Give a bounding box for every parasitised red blood cell.
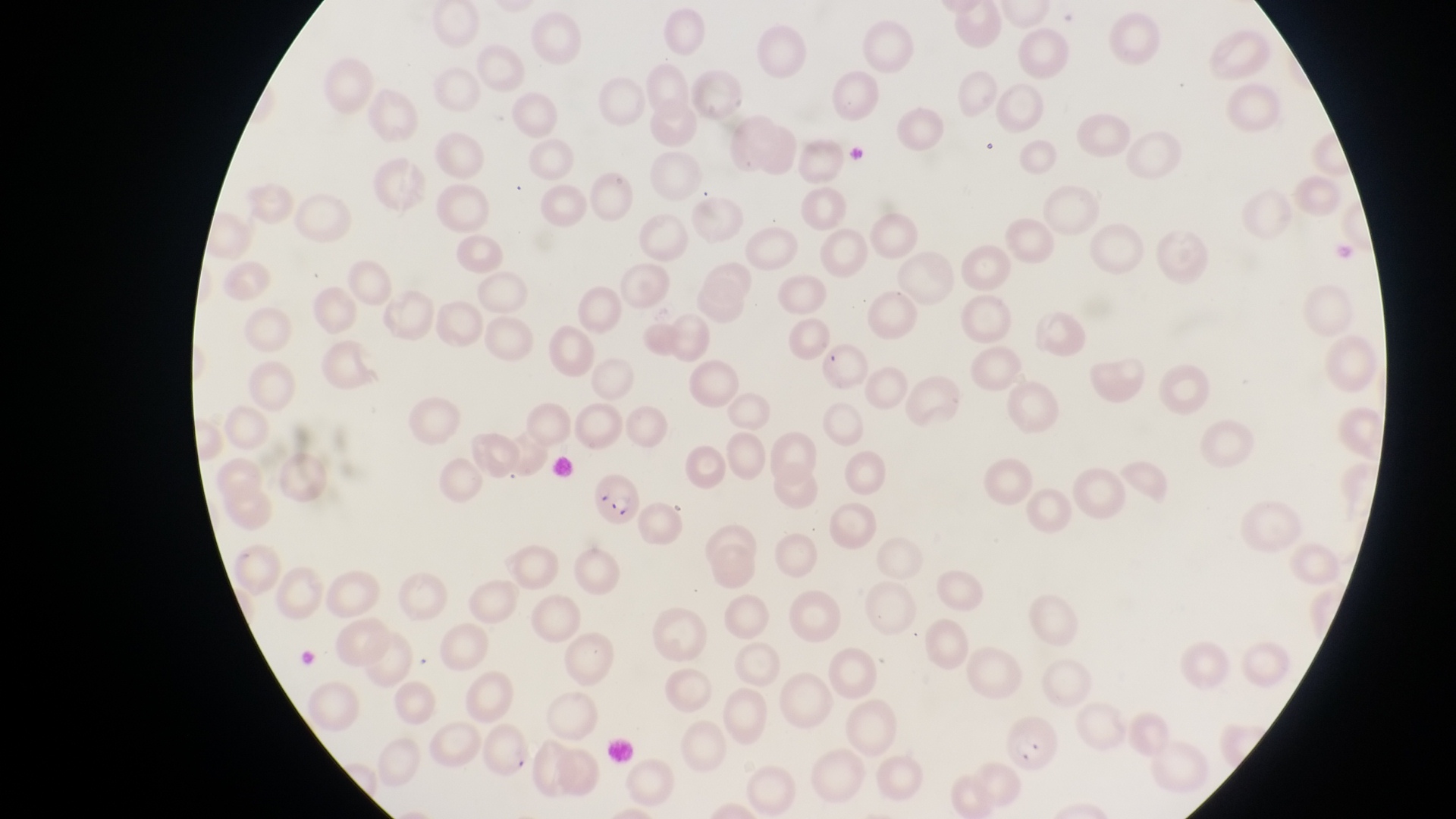
Approximate bounding boxes as left top right bottom in pixels.
Parasitised red blood cells: 587 470 642 529.

Summary:
  - Magnification: 1000x
  - Preparation: thin blood film
  - Capture: smartphone photograph through the eyepiece of an Olympus CX-23 microscope
  - Country: Uganda
  - Field of view: single
  - Image size: 1456×819 pixels